Classify this cell by malaria status.
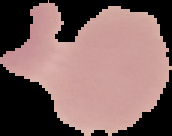
Uninfected.

preparation = thin blood smear
image type = cell region segmented out of the field of view; surrounding area masked to black
image size = 172×136 pixels